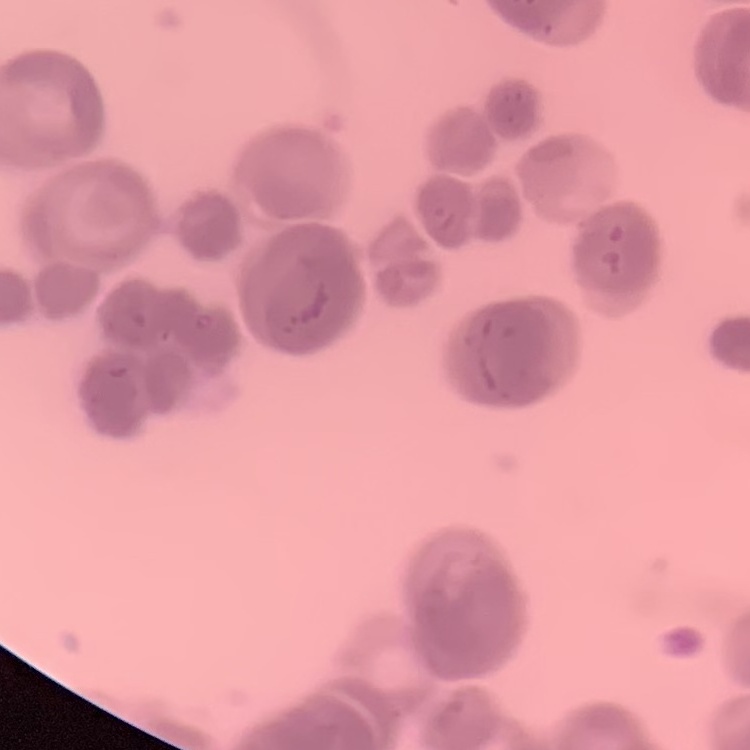 The erythrocytes exhibit rouleaux formation. Thin blood film. Stained with either Field's or Giemsa. One tile cut from a larger photomicrograph.